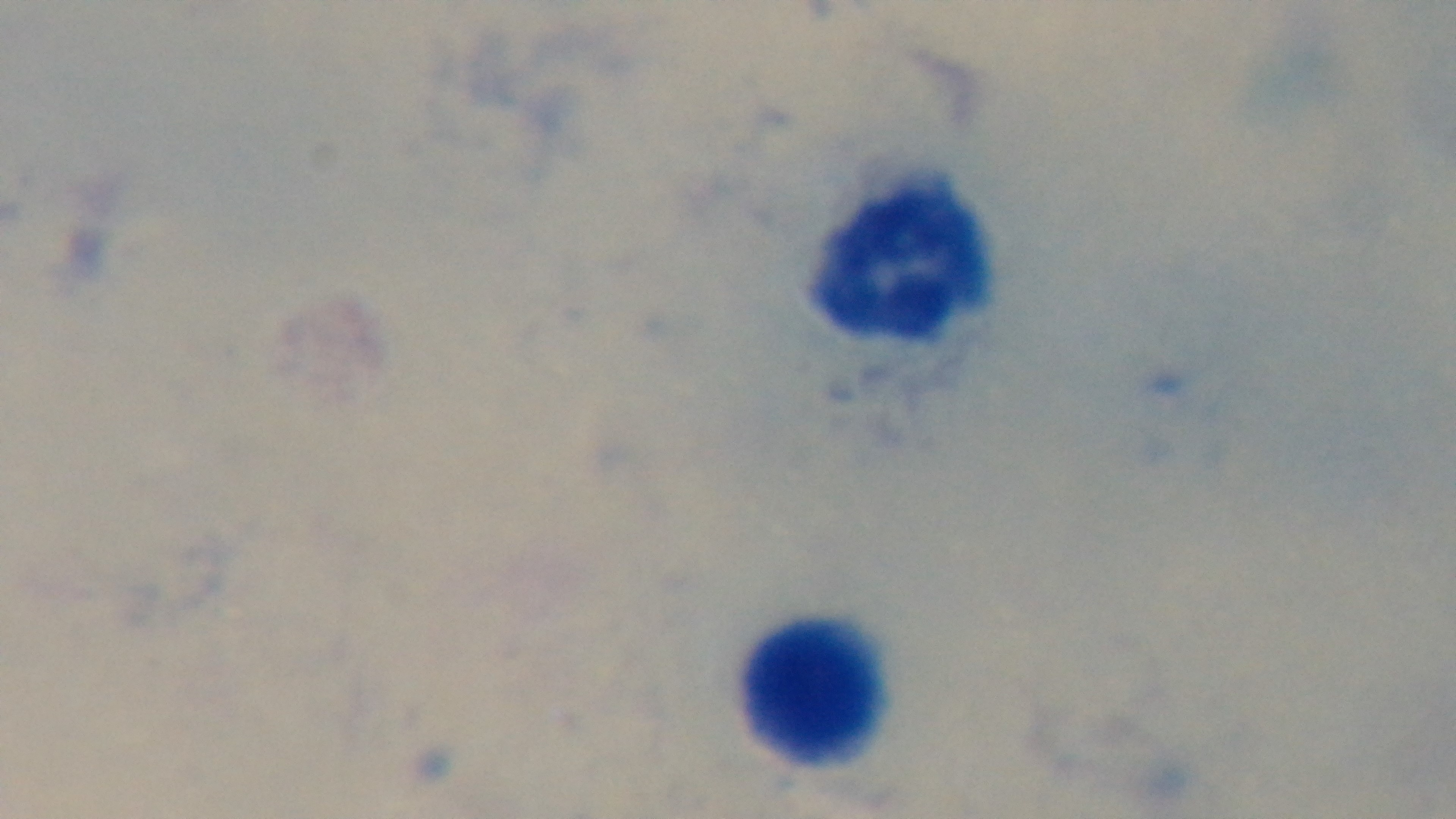

Summary:
  - Malaria status: negative
  - Preparation: thick
  - Capture: mounted 4K digital camera
  - Objective: 100x oil immersion
  - Field of view: one from the slide
  - Modality: light microscopy
  - Stain: Giemsa